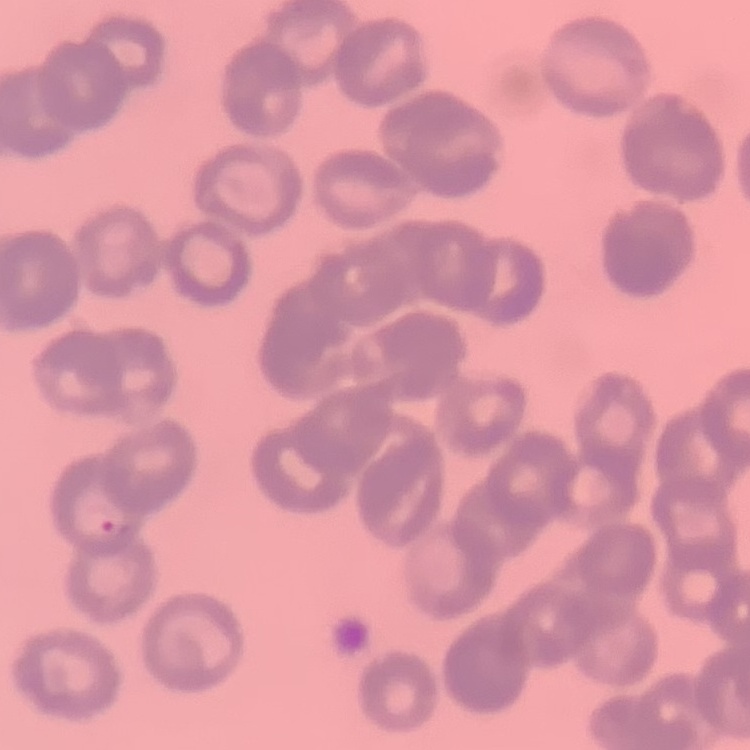

Summary:
  - Red blood cell morphology: rouleaux formation
  - Preparation: thin blood smear
  - Stain: Field's or Giemsa
  - Image type: one tile cut from a larger photomicrograph